Give the preparation type.
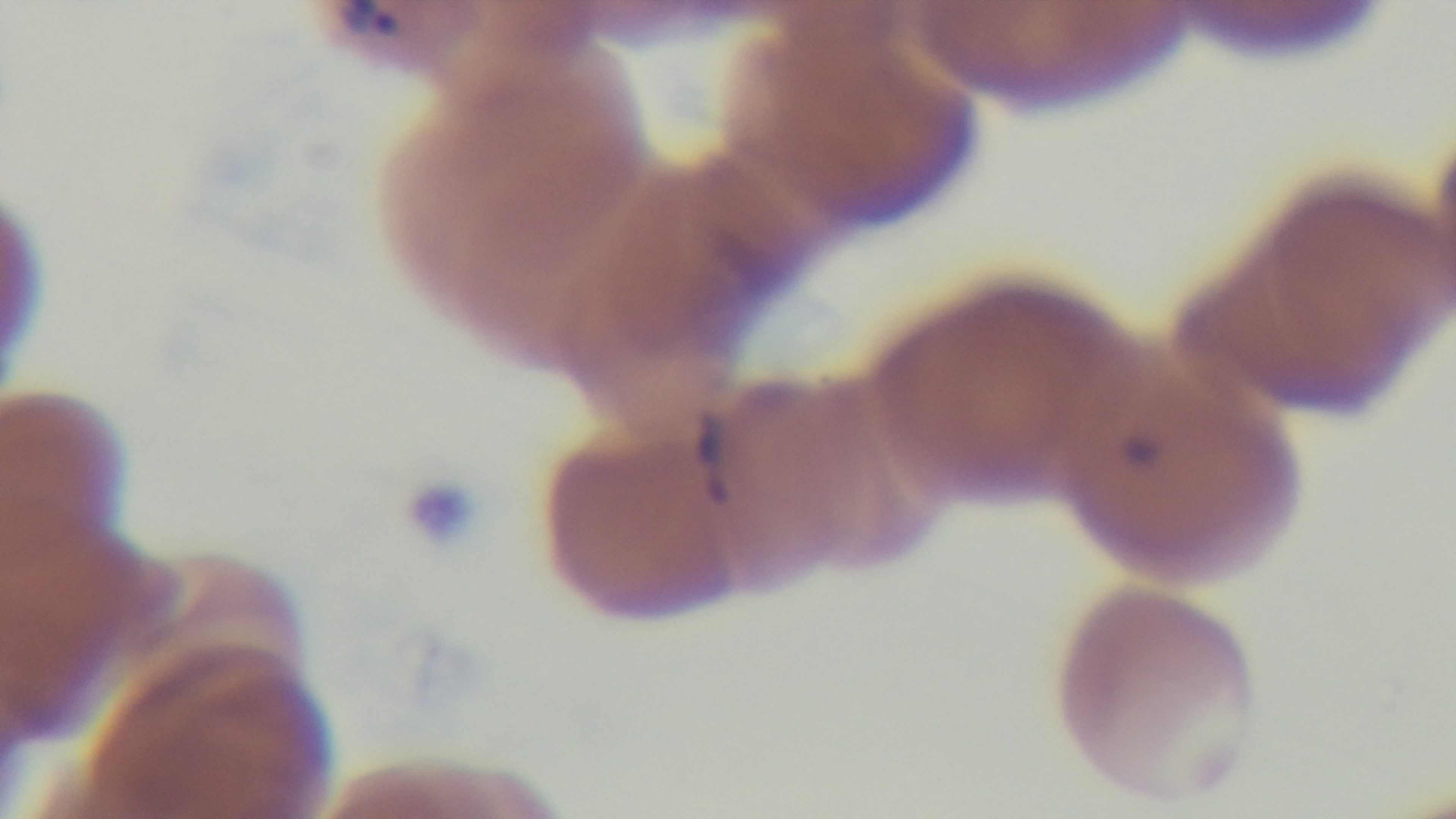
A thin smear.

Summary:
  - Stain: Giemsa
  - Modality: light microscopy
  - Malaria status: positive
  - Objective: 100x oil immersion
  - Capture: mounted 4K digital camera
  - Field of view: single